Outline each Plasmodium malariae-infected red blood cell.
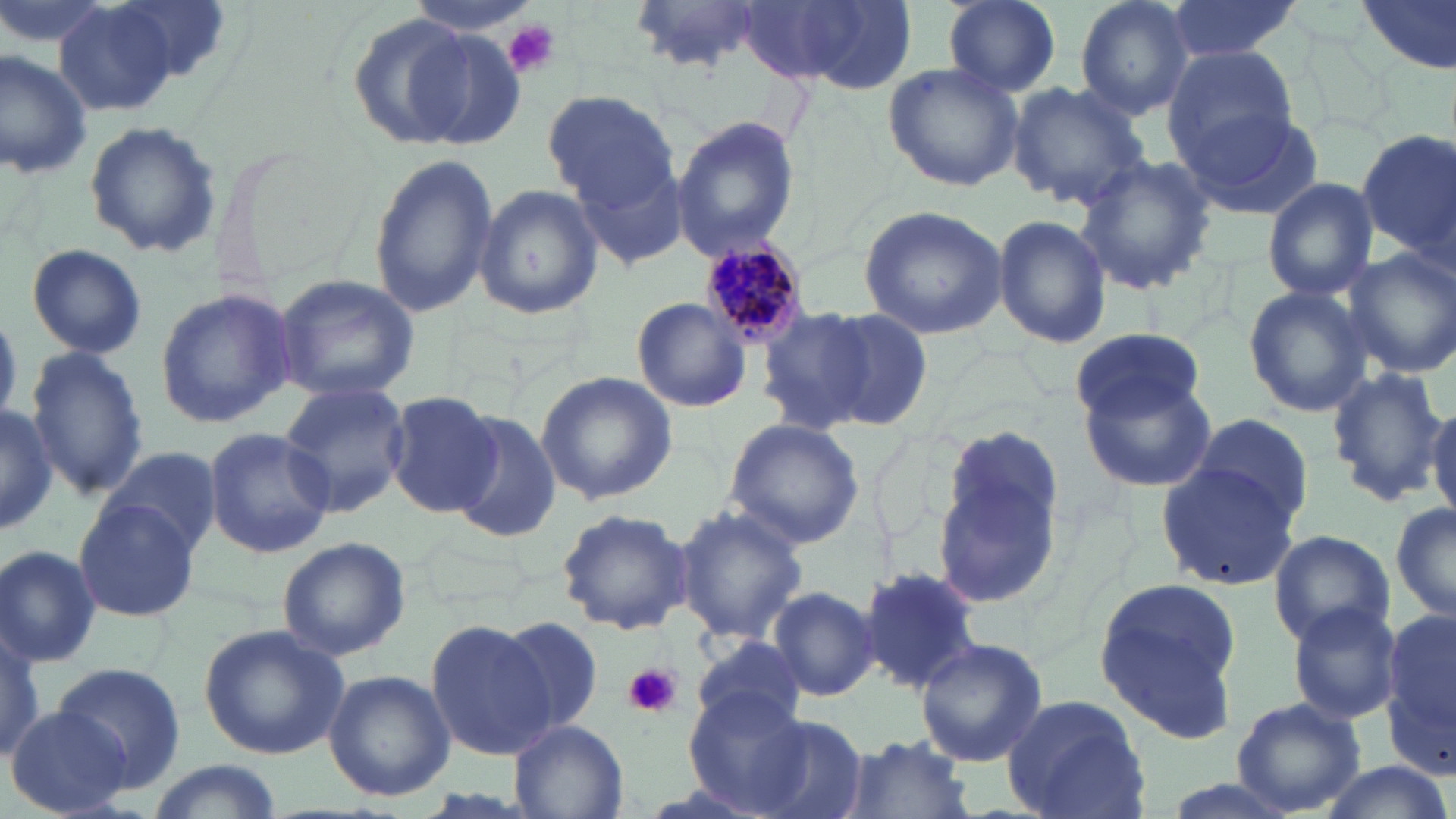
Approximate bounding boxes as (x1,y1)-(x2,y2) corner pairs in pixels.
Plasmodium malariae-infected red blood cells: (697,236)-(813,346).

slide-level diagnosis = Plasmodium malariae
image size = 1456×819 pixels
platelet locations = approximate bounding boxes as (x1,y1)-(x2,y2) corner pairs in pixels: (501,19)-(562,80), (624,662)-(681,719)
preparation = thin blood film
modality = light microscopy
magnification = 1000x
stain = May-Grünwald-Giemsa
uninfected red blood cell locations = approximate bounding boxes as (x1,y1)-(x2,y2) corner pairs in pixels: (0,0)-(118,55), (52,0)-(185,116), (403,0)-(540,37), (629,0)-(765,71), (942,0)-(1062,96), (1074,0)-(1196,120), (1161,0)-(1307,65), (1355,0)-(1456,81), (742,2)-(910,91), (344,12)-(483,148), (403,28)-(528,149), (1161,44)-(1298,170), (0,46)-(92,177), (884,61)-(1027,191), (1005,82)-(1150,211), (541,89)-(681,211), (1176,105)-(1325,221), (672,117)-(802,259), (83,122)-(223,256), (1356,130)-(1456,264), (568,143)-(693,276), (366,153)-(498,317), (1072,156)-(1218,294), (1262,178)-(1378,300), (473,184)-(602,320), (858,204)-(1011,340), (992,213)-(1110,349), (26,243)-(147,359), (1345,248)-(1456,378), (273,273)-(420,405), (1243,284)-(1371,416), (153,286)-(297,431), (632,297)-(753,414), (755,306)-(881,433), (820,307)-(935,431), (1069,327)-(1206,425), (24,346)-(147,502), (1325,364)-(1449,506), (536,371)-(678,504), (1077,371)-(1217,495), (280,381)-(411,516), (386,389)-(502,515), (1427,398)-(1456,519), (0,404)-(56,536), (1189,411)-(1314,529), (446,413)-(560,544), (723,418)-(864,550), (201,425)-(337,559), (933,429)-(1066,611), (101,444)-(221,558), (1154,459)-(1301,595), (1390,498)-(1456,625), (74,499)-(200,624), (672,503)-(808,645), (556,508)-(693,636), (1267,529)-(1394,648), (276,536)-(411,663), (0,542)-(102,668), (858,568)-(984,693), (1091,574)-(1247,744), (768,586)-(880,701), (1286,602)-(1401,726), (1383,603)-(1456,774), (496,616)-(608,735), (0,617)-(44,764), (425,620)-(557,760), (198,624)-(350,761), (694,635)-(808,736), (916,635)-(1048,767), (52,661)-(187,794), (324,671)-(455,801), (684,693)-(811,814), (1003,695)-(1149,819), (1232,698)-(1365,816), (6,705)-(131,817), (748,716)-(871,819), (510,719)-(628,819), (843,733)-(974,819), (144,759)-(283,819), (1313,760)-(1454,819)
field of view = single